Describe the morphology of the erythrocytes.
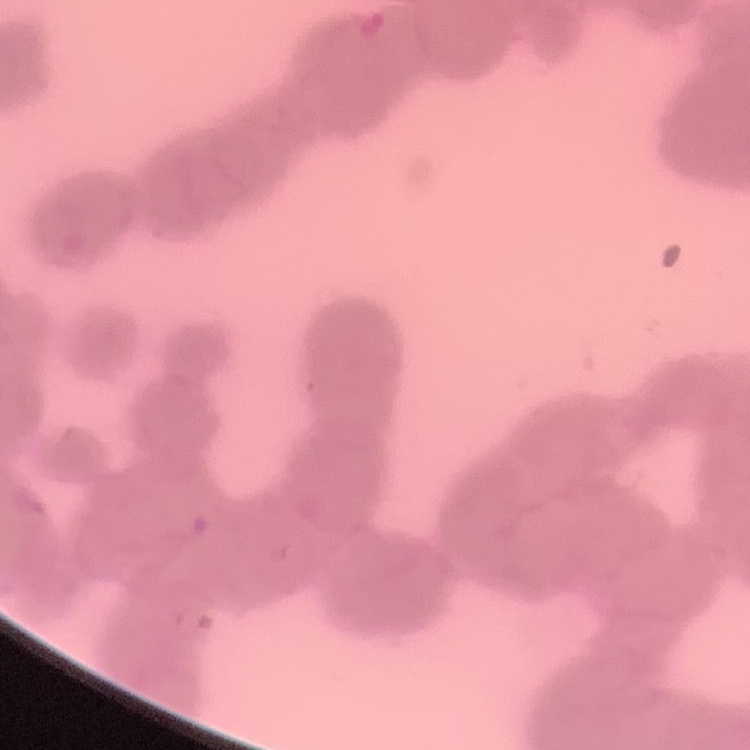

They show rouleaux formation.

Field's or Giemsa stain. Thin blood smear. Square crop of a larger photomicrograph.